Assess this cell for malaria.
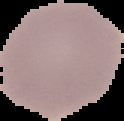
Uninfected.

Summary:
  - Preparation: thin blood smear
  - Image type: segmented cell region on a black background
  - Image size: 124×121 pixels